Outline each blood parasite and name the species.
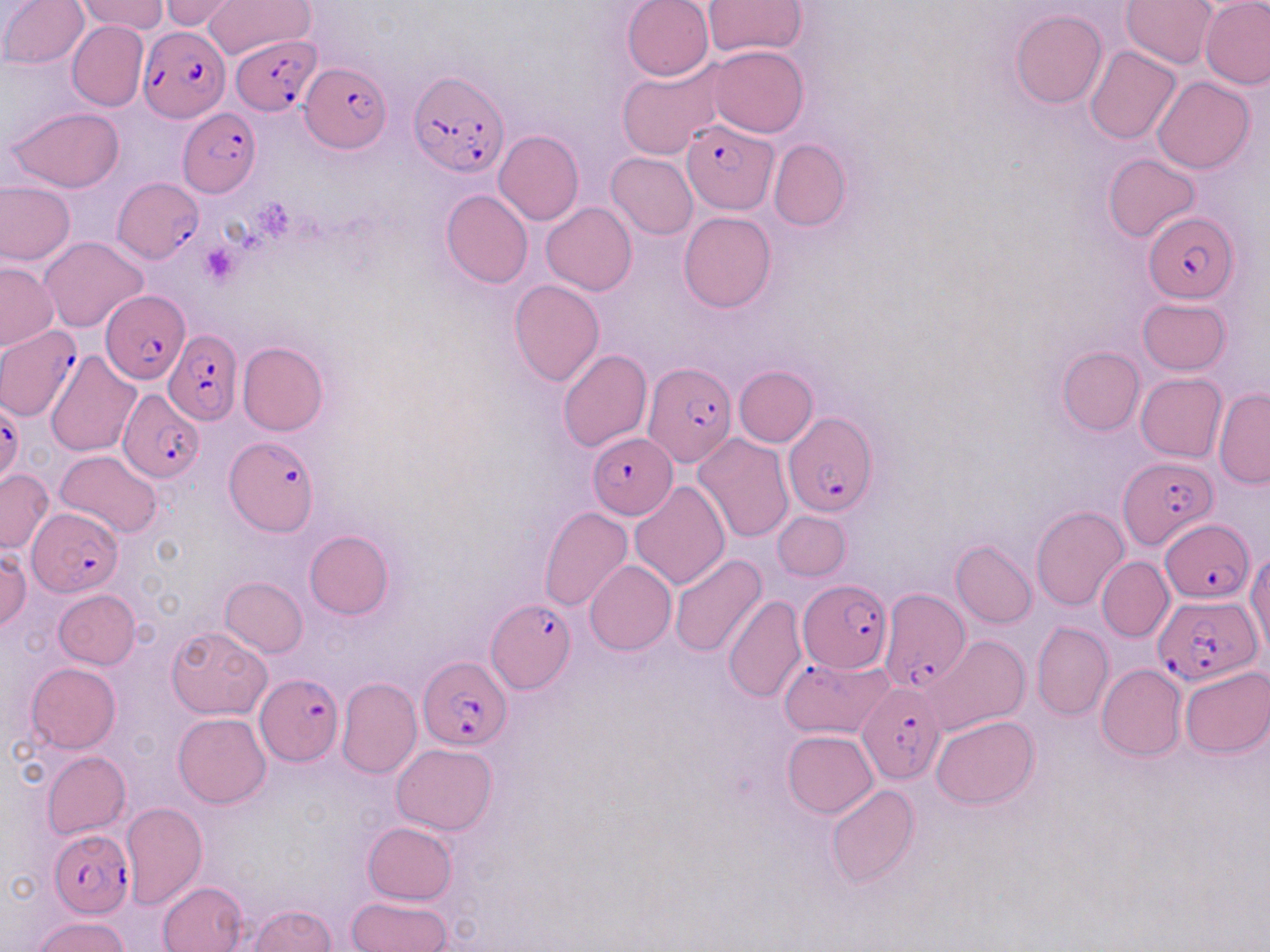
Approximate bounding boxes as [x1, y1, x2, y2] in pixels.
Plasmodium falciparum-infected red blood cells: [138, 26, 230, 122], [230, 35, 322, 116], [299, 60, 391, 153], [409, 69, 508, 177], [177, 107, 261, 196], [679, 118, 777, 215], [112, 176, 204, 264], [1144, 212, 1240, 303], [101, 290, 190, 383], [0, 325, 83, 422], [163, 327, 241, 425], [644, 361, 739, 466], [118, 388, 205, 480], [0, 397, 24, 492], [784, 411, 877, 517], [587, 434, 676, 518], [225, 438, 319, 535], [1119, 454, 1215, 550], [28, 508, 123, 596], [1159, 518, 1254, 602], [799, 579, 893, 672], [882, 589, 970, 696], [1153, 594, 1261, 686], [487, 599, 576, 693], [417, 657, 513, 750], [255, 674, 343, 765], [858, 681, 945, 785], [47, 827, 133, 918].
No Plasmodium ovale, Plasmodium malariae, Plasmodium vivax, Babesia divergens, or Trypanosoma brucei observed.

Platelet locations: [198, 243, 239, 284]. Uninfected red blood cell locations: [1, 0, 89, 69], [77, 0, 168, 34], [160, 0, 241, 29], [203, 0, 312, 58], [623, 0, 714, 81], [703, 0, 808, 56], [1121, 1, 1218, 69], [1201, 1, 1270, 89], [1009, 10, 1108, 109], [67, 20, 148, 112], [708, 44, 807, 137], [1085, 46, 1181, 146], [616, 60, 725, 160], [1150, 76, 1255, 173], [8, 106, 124, 193], [495, 130, 583, 225], [769, 139, 851, 231], [607, 152, 698, 239], [1103, 153, 1200, 241], [0, 183, 75, 265], [441, 190, 533, 289], [541, 203, 638, 295], [678, 212, 776, 312], [40, 236, 148, 333], [1, 262, 58, 350], [509, 279, 605, 387], [1137, 298, 1230, 375], [237, 342, 328, 436], [1057, 346, 1144, 435], [558, 349, 653, 452], [45, 350, 141, 458], [734, 365, 817, 447], [1136, 373, 1227, 463], [1214, 389, 1270, 489], [694, 432, 794, 543], [55, 450, 163, 539], [0, 469, 52, 553], [630, 482, 730, 590], [1030, 505, 1129, 609], [540, 507, 633, 611], [773, 511, 851, 581], [305, 530, 394, 620], [952, 540, 1037, 629], [0, 548, 31, 633], [1247, 550, 1270, 660], [668, 555, 767, 659], [1097, 556, 1174, 643], [584, 560, 677, 655], [221, 577, 307, 657], [54, 589, 140, 669], [723, 594, 808, 703], [1032, 622, 1113, 721], [166, 626, 271, 719], [925, 635, 1030, 734], [779, 654, 893, 738], [26, 663, 121, 753], [1096, 664, 1186, 760], [1179, 665, 1270, 757], [336, 677, 422, 779], [173, 712, 271, 806], [931, 715, 1037, 809], [782, 729, 879, 818], [391, 744, 497, 835], [42, 751, 130, 839], [826, 785, 920, 887], [121, 801, 207, 909], [362, 821, 457, 904], [158, 881, 247, 952], [346, 896, 452, 952], [247, 905, 337, 951], [32, 916, 130, 952]. Slide-level diagnosis: Plasmodium falciparum. One field of a larger specimen. Captured at 1000x magnification. Image is 1270×952 pixels. May-Grünwald-Giemsa stain. Optical microscopy. Thin blood smear.